Outline each blood parasite and name the species.
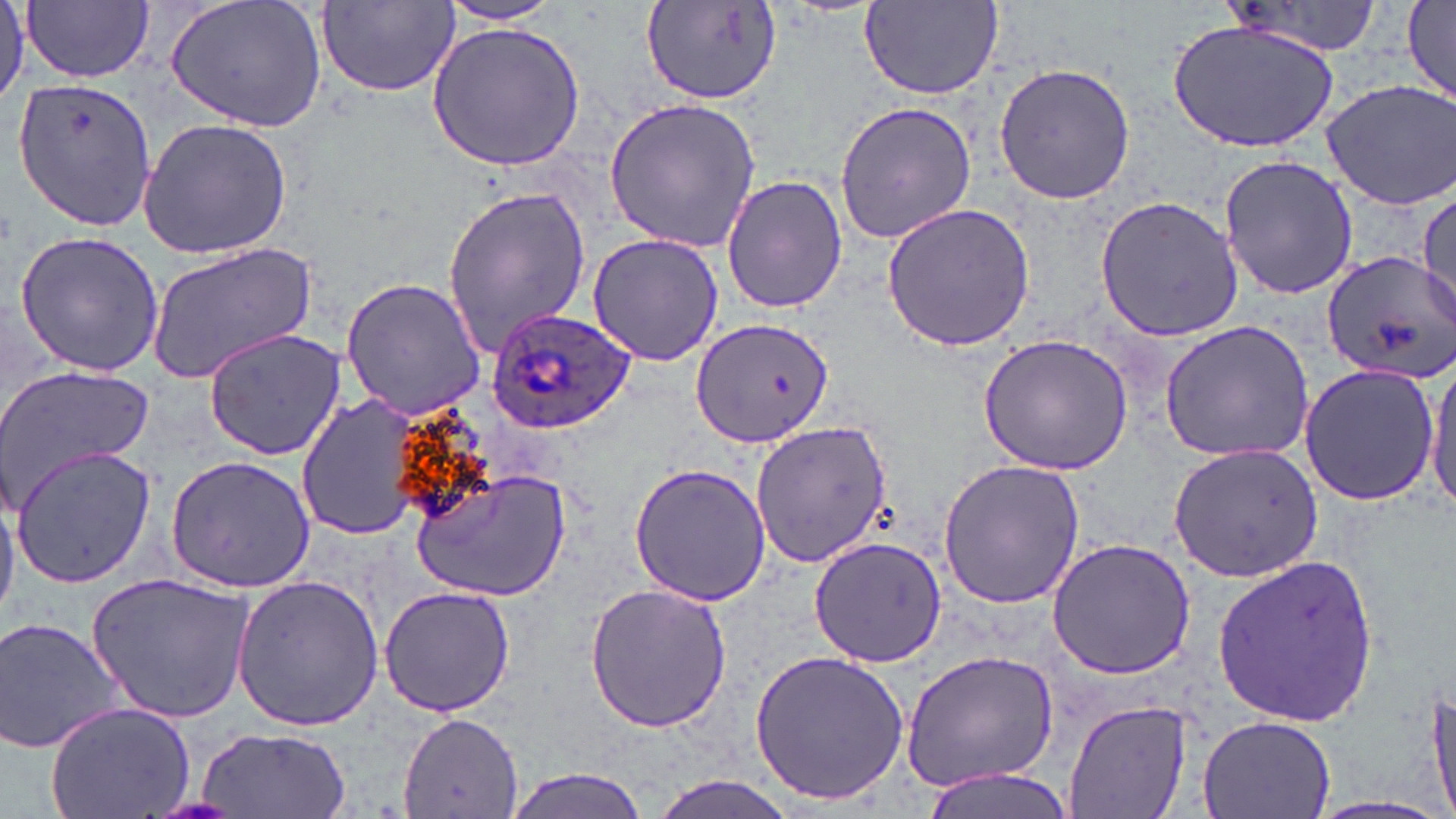

Approximate bounding boxes as (x1,y1)-(x2,y2) corner pairs in pixels.
Plasmodium ovale-infected red blood cells: (485,306)-(637,433).
No Plasmodium falciparum, Plasmodium malariae, Plasmodium vivax, Babesia divergens, or Trypanosoma brucei observed.

Uninfected red blood cell locations: (23,0)-(154,83), (166,0)-(326,134), (316,1)-(461,98), (1400,1)-(1455,101), (640,2)-(783,105), (858,2)-(1005,100), (436,3)-(568,29), (1169,18)-(1339,154), (426,21)-(587,170), (993,61)-(1137,202), (13,79)-(155,229), (1321,80)-(1456,210), (603,98)-(762,255), (833,99)-(977,244), (135,118)-(295,259), (1218,154)-(1358,301), (722,173)-(846,314), (441,183)-(591,359), (1416,187)-(1456,323), (1094,195)-(1245,342), (880,201)-(1035,350), (13,229)-(165,377), (587,234)-(725,368), (146,243)-(317,381), (1323,251)-(1456,384), (341,275)-(486,418), (687,317)-(834,449), (1158,318)-(1316,463), (203,327)-(345,461), (977,332)-(1135,475), (1426,354)-(1456,516), (1296,363)-(1440,506), (0,368)-(154,510), (298,393)-(429,543), (750,419)-(892,569), (1168,442)-(1322,579), (10,447)-(158,587), (165,455)-(316,593), (937,458)-(1086,609), (629,462)-(772,604), (410,467)-(573,601), (0,482)-(20,620), (808,536)-(950,668), (1046,537)-(1197,679), (1211,553)-(1380,731), (86,575)-(256,725), (230,575)-(384,733), (584,581)-(735,735), (378,586)-(517,717), (1,614)-(127,756), (900,647)-(1062,794), (747,649)-(913,806), (1427,675)-(1456,819), (1065,699)-(1192,819), (46,701)-(195,819), (399,711)-(522,816), (1197,713)-(1335,819), (192,727)-(354,819), (914,767)-(1079,819), (500,769)-(652,819), (644,774)-(810,819), (1298,796)-(1456,819). Slide-level diagnosis: Plasmodium ovale. Captured at 1000x magnification. Image is 1456×819 pixels. One field of a larger specimen. May-Grünwald-Giemsa-stained preparation. Thin blood film. Optical microscopy.